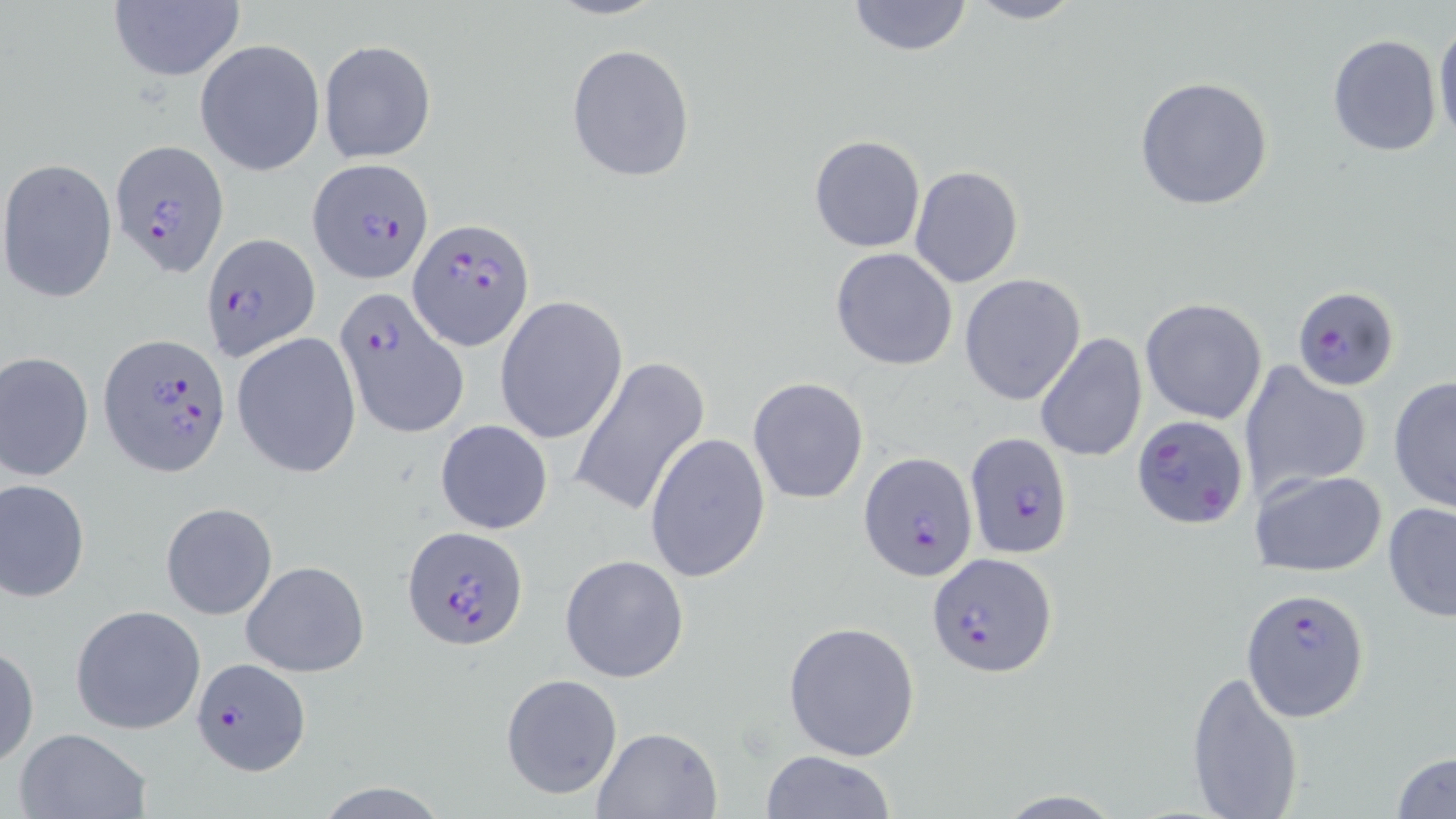

Summary:
  - Coordinate format: approximate bounding boxes as (x1, y1, x2, y2) in pixels
  - Uninfected red blood cell locations: (547, 0, 666, 21), (961, 0, 1085, 25), (104, 1, 246, 85), (846, 1, 973, 56), (1433, 18, 1456, 146), (1327, 33, 1442, 158), (195, 39, 327, 176), (318, 39, 437, 164), (565, 43, 696, 183), (1133, 76, 1275, 212), (810, 135, 926, 253), (1, 158, 118, 302), (909, 166, 1024, 287), (831, 246, 959, 371), (959, 274, 1086, 405), (494, 296, 628, 445), (1141, 298, 1267, 423), (231, 331, 362, 478), (1034, 331, 1145, 462), (1, 350, 94, 482), (571, 355, 709, 518), (1240, 362, 1370, 501), (1387, 374, 1456, 514), (748, 377, 868, 504), (435, 419, 554, 534), (643, 431, 770, 585), (1249, 469, 1388, 578), (1, 478, 92, 602), (160, 502, 278, 621), (1382, 502, 1456, 622), (558, 553, 691, 684), (241, 560, 369, 678), (70, 604, 206, 735), (783, 620, 921, 761), (0, 643, 38, 768), (1185, 668, 1305, 819), (501, 673, 623, 800), (590, 726, 723, 819), (12, 727, 151, 819), (757, 750, 896, 819), (1390, 750, 1456, 818)
  - Plasmodium falciparum-infected red blood cell locations: (109, 139, 228, 277), (308, 158, 433, 282), (409, 218, 535, 354), (204, 233, 321, 360), (1291, 285, 1400, 391), (332, 287, 469, 443), (100, 334, 231, 474), (1132, 414, 1249, 529), (963, 432, 1075, 559), (858, 451, 981, 583), (402, 525, 528, 650), (928, 552, 1060, 677), (1244, 588, 1370, 722), (189, 655, 310, 778)
  - Slide-level diagnosis: Plasmodium falciparum
  - Modality: optical microscopy
  - Stain: May-Grünwald-Giemsa
  - Image size: 1456×819 pixels
  - Magnification: 1000x
  - Field of view: one of a larger specimen
  - Preparation: thin blood film